Locate the cells, classifying each as a parasitized red blood cell, an uninfected red blood cell, or a white blood cell.
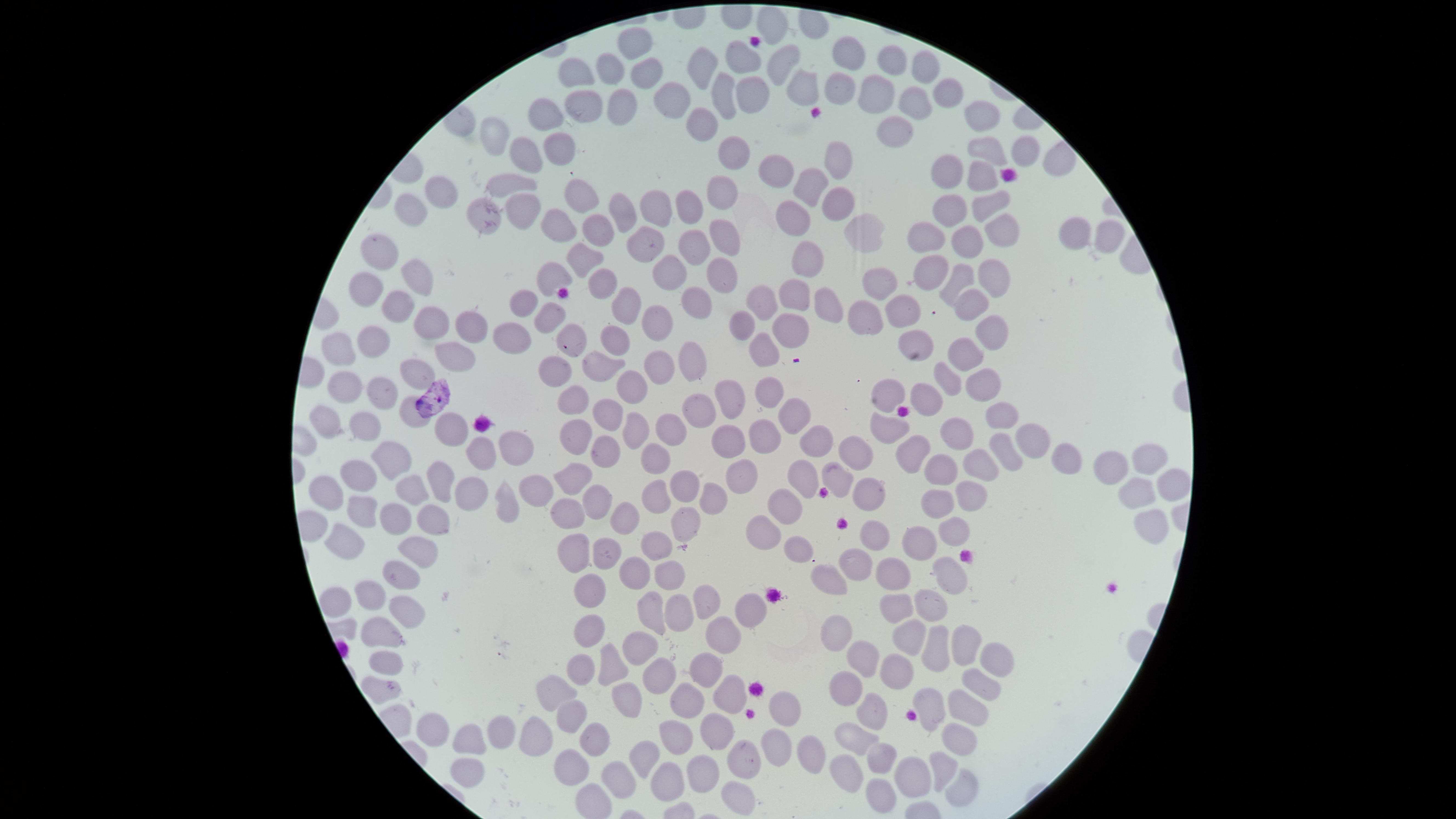

No parasitized red blood cells identified.
Approximate marker points, in pixels from the top-left corner.
Uninfected red blood cells: (x=771, y=21), (x=632, y=42), (x=742, y=53), (x=849, y=56), (x=780, y=58), (x=887, y=59), (x=704, y=64), (x=609, y=68), (x=642, y=68), (x=923, y=70), (x=572, y=73), (x=803, y=85), (x=839, y=87), (x=752, y=89), (x=725, y=92), (x=669, y=96), (x=915, y=96), (x=874, y=97), (x=946, y=97), (x=618, y=103), (x=583, y=109), (x=546, y=115), (x=978, y=116), (x=705, y=123), (x=894, y=126), (x=491, y=139), (x=556, y=147), (x=989, y=149), (x=735, y=150), (x=1021, y=150), (x=529, y=151), (x=838, y=159), (x=773, y=166), (x=947, y=166), (x=978, y=176), (x=509, y=185), (x=805, y=188), (x=722, y=189), (x=442, y=191), (x=586, y=199), (x=986, y=200), (x=657, y=206), (x=836, y=207), (x=692, y=208), (x=480, y=209), (x=623, y=209), (x=950, y=209), (x=409, y=211), (x=523, y=211), (x=552, y=221), (x=794, y=224), (x=862, y=228), (x=1069, y=231), (x=718, y=232), (x=998, y=233), (x=589, y=236), (x=920, y=236), (x=1105, y=236), (x=964, y=239), (x=645, y=241), (x=692, y=247), (x=377, y=252), (x=578, y=257), (x=813, y=262), (x=930, y=270), (x=414, y=274), (x=718, y=276), (x=548, y=278), (x=675, y=278), (x=597, y=279), (x=987, y=279), (x=958, y=280), (x=880, y=284), (x=369, y=288), (x=794, y=298), (x=967, y=302), (x=622, y=304), (x=761, y=304), (x=398, y=305), (x=698, y=305), (x=521, y=306), (x=825, y=306), (x=549, y=311), (x=907, y=312), (x=866, y=316), (x=433, y=324), (x=658, y=324), (x=742, y=325), (x=986, y=327), (x=467, y=330), (x=509, y=332), (x=789, y=335), (x=568, y=338), (x=620, y=338), (x=372, y=341), (x=915, y=346), (x=344, y=348), (x=967, y=350), (x=765, y=351), (x=451, y=357), (x=690, y=359), (x=552, y=362), (x=654, y=363), (x=605, y=367), (x=947, y=376), (x=417, y=377), (x=981, y=383), (x=572, y=385), (x=347, y=386), (x=632, y=391), (x=765, y=391), (x=729, y=394), (x=886, y=394), (x=378, y=397), (x=926, y=399), (x=608, y=405), (x=410, y=413), (x=706, y=413), (x=997, y=416), (x=789, y=417), (x=366, y=422), (x=331, y=424), (x=675, y=426), (x=443, y=429), (x=636, y=429), (x=887, y=429), (x=759, y=431), (x=954, y=431), (x=579, y=432), (x=1024, y=435), (x=729, y=443), (x=814, y=443), (x=1004, y=448), (x=517, y=449), (x=603, y=450), (x=857, y=450), (x=485, y=451), (x=907, y=451), (x=1056, y=457), (x=387, y=458), (x=657, y=461), (x=1149, y=461), (x=1104, y=466), (x=981, y=467), (x=927, y=469), (x=834, y=472), (x=801, y=473), (x=356, y=474), (x=736, y=476), (x=568, y=477), (x=1172, y=480), (x=436, y=481), (x=684, y=482), (x=406, y=488), (x=967, y=492), (x=533, y=493), (x=871, y=494), (x=1133, y=494), (x=325, y=495), (x=653, y=495), (x=468, y=496), (x=709, y=500), (x=938, y=500), (x=503, y=503), (x=595, y=503), (x=355, y=505), (x=783, y=507), (x=566, y=514), (x=617, y=514), (x=1150, y=518), (x=396, y=520), (x=434, y=521), (x=681, y=522), (x=766, y=528), (x=950, y=528), (x=877, y=535), (x=333, y=540), (x=922, y=541), (x=656, y=548), (x=417, y=552), (x=575, y=552), (x=606, y=552), (x=798, y=552), (x=855, y=563), (x=635, y=571), (x=401, y=573), (x=894, y=573), (x=943, y=573), (x=661, y=577), (x=829, y=580), (x=372, y=594), (x=585, y=594), (x=335, y=600), (x=710, y=604), (x=922, y=606), (x=649, y=608), (x=680, y=609), (x=898, y=609), (x=746, y=612), (x=406, y=616), (x=589, y=626), (x=836, y=626), (x=720, y=631), (x=381, y=632), (x=907, y=634), (x=958, y=639), (x=936, y=648), (x=637, y=650), (x=864, y=655), (x=608, y=660), (x=383, y=665), (x=987, y=666), (x=575, y=667), (x=894, y=667), (x=698, y=670), (x=656, y=675), (x=844, y=680), (x=971, y=686), (x=380, y=689), (x=728, y=693), (x=552, y=694), (x=632, y=701), (x=685, y=702), (x=930, y=702), (x=963, y=707), (x=784, y=708), (x=571, y=715), (x=870, y=716), (x=718, y=727), (x=429, y=729), (x=501, y=729), (x=672, y=733), (x=950, y=735), (x=853, y=736), (x=534, y=737), (x=464, y=743), (x=593, y=743), (x=640, y=746), (x=769, y=747), (x=815, y=753), (x=878, y=759), (x=744, y=760), (x=567, y=765), (x=942, y=767), (x=702, y=769), (x=845, y=770), (x=464, y=771), (x=665, y=775), (x=907, y=777), (x=613, y=778), (x=959, y=786), (x=735, y=788), (x=870, y=795).
No white blood cells identified.

Summary:
  - Field of view: single
  - Visible region: circular
  - Preparation: thin blood smear
  - Capture: smartphone photograph through the microscope eyepiece
  - Image size: 1456×819 pixels
  - Stain: Giemsa